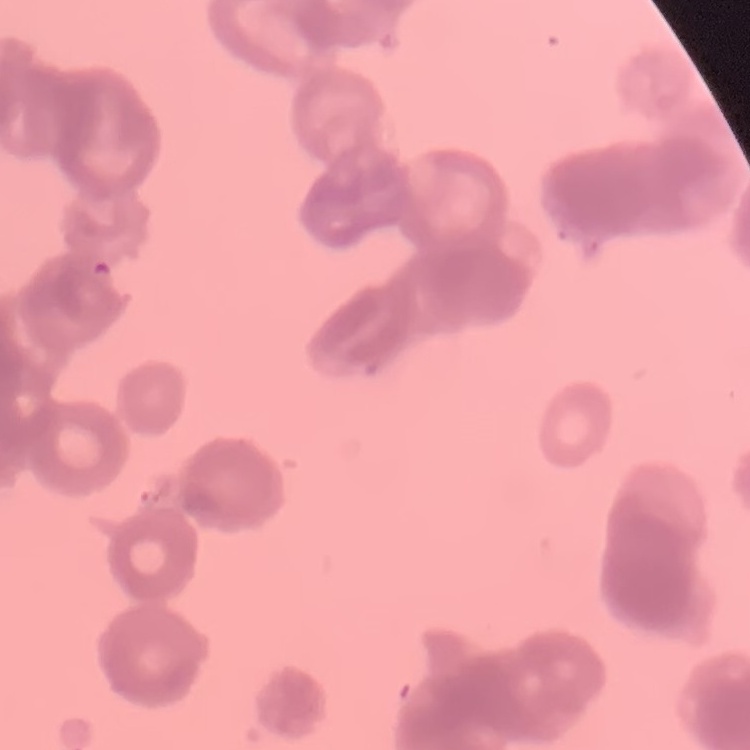
Summary:
  - Erythrocyte morphology: rouleaux formation
  - Preparation: thin peripheral smear
  - Stain: Field's or Giemsa
  - Image type: square crop of a larger photomicrograph